Locate leukocytes (white blood cells).
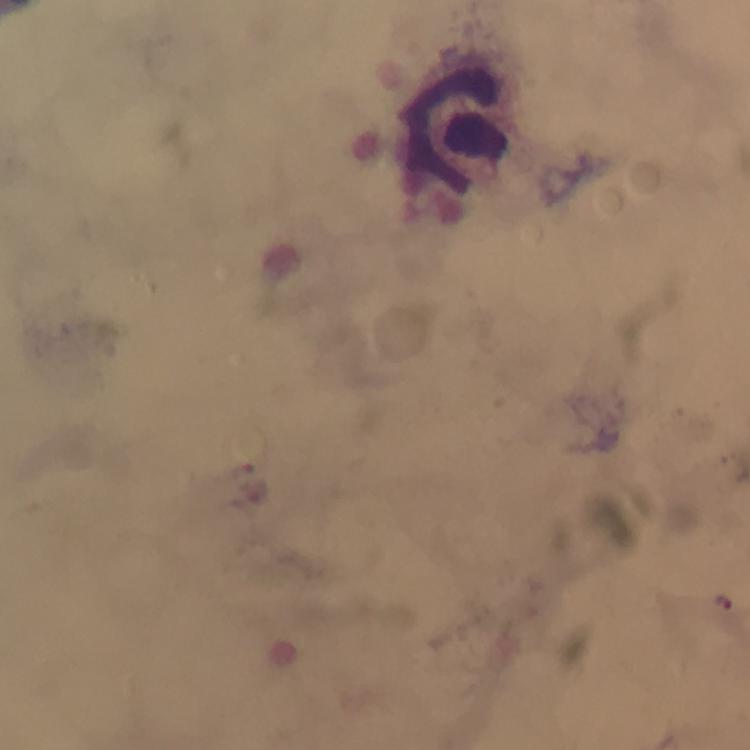
Approximate centers as (x, y) in pixels.
Leukocytes: (464, 127).

Summary:
  - Plasmodium parasite locations: (254, 492), (723, 603)
  - Stain: Giemsa
  - Magnification: 100x
  - Preparation: thick blood smear
  - Context: from a malaria diagnostic workup
  - Capture: smartphone mounted on the microscope
  - Image size: 750×750 pixels
  - Cropped from: a single field of view
  - Immersion oil: applied